Locate every Plasmodium malariae-infected red blood cell.
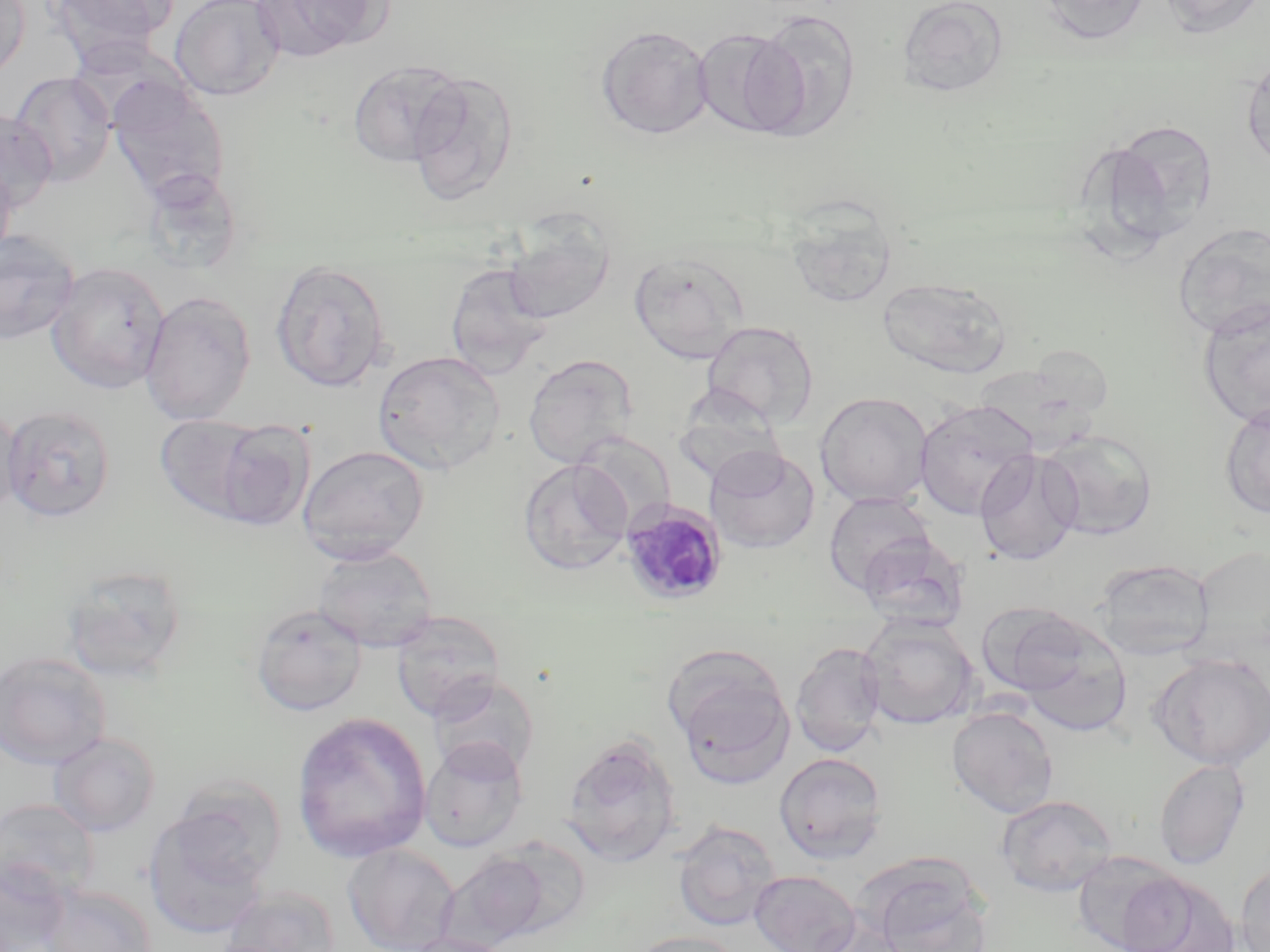

Approximate bounding boxes as (x1, y1, x2, y2) in pixels.
Plasmodium malariae-infected red blood cells: (618, 499, 728, 606).

Uninfected red blood cell locations: (0, 0, 31, 82), (46, 0, 180, 59), (170, 0, 285, 101), (253, 0, 391, 60), (897, 0, 1010, 99), (1036, 0, 1151, 45), (1156, 0, 1265, 38), (750, 10, 861, 137), (596, 25, 714, 139), (692, 28, 805, 139), (1243, 58, 1270, 171), (347, 59, 466, 167), (406, 70, 520, 206), (9, 71, 117, 186), (106, 75, 230, 203), (0, 109, 57, 212), (1103, 121, 1218, 245), (0, 160, 17, 264), (138, 167, 246, 275), (783, 200, 901, 309), (502, 214, 616, 326), (1173, 222, 1270, 339), (0, 231, 81, 345), (629, 251, 748, 363), (270, 259, 392, 393), (46, 261, 170, 393), (445, 263, 552, 378), (877, 277, 1013, 378), (139, 291, 256, 425), (1197, 298, 1270, 428), (701, 320, 819, 428), (373, 350, 506, 475), (523, 354, 637, 467), (815, 392, 933, 507), (914, 399, 1039, 520), (1219, 401, 1270, 519), (0, 402, 23, 519), (2, 404, 116, 523), (154, 414, 264, 521), (213, 420, 315, 530), (1039, 430, 1159, 541), (573, 431, 676, 530), (297, 444, 430, 563), (705, 447, 820, 554), (974, 449, 1082, 566), (518, 458, 633, 576), (823, 492, 937, 595), (312, 545, 439, 652), (1093, 559, 1215, 660), (60, 562, 189, 683), (976, 602, 1091, 696), (250, 603, 368, 717), (391, 611, 507, 722), (1013, 614, 1133, 736), (859, 615, 979, 730), (790, 641, 886, 756), (0, 650, 112, 770), (1149, 652, 1270, 770), (673, 667, 794, 790), (425, 674, 539, 780), (947, 705, 1059, 817), (290, 711, 432, 864), (48, 732, 161, 837), (561, 734, 681, 867), (419, 738, 528, 852), (774, 752, 888, 863), (1153, 758, 1251, 869), (996, 794, 1118, 897), (0, 797, 101, 902), (142, 805, 271, 941), (672, 819, 782, 931), (343, 844, 460, 952), (439, 850, 551, 949), (1071, 850, 1187, 952), (0, 861, 73, 952), (1236, 862, 1270, 952), (864, 865, 992, 952), (749, 870, 862, 952), (1119, 873, 1241, 952), (40, 884, 157, 952), (221, 885, 341, 952), (809, 918, 913, 952), (628, 930, 747, 952), (399, 932, 517, 952). Slide-level diagnosis: Plasmodium malariae. May-Grünwald-Giemsa stain. Image is 1270×952 pixels. Single field of view. Thin blood film. Light microscopy. 1000x magnification.